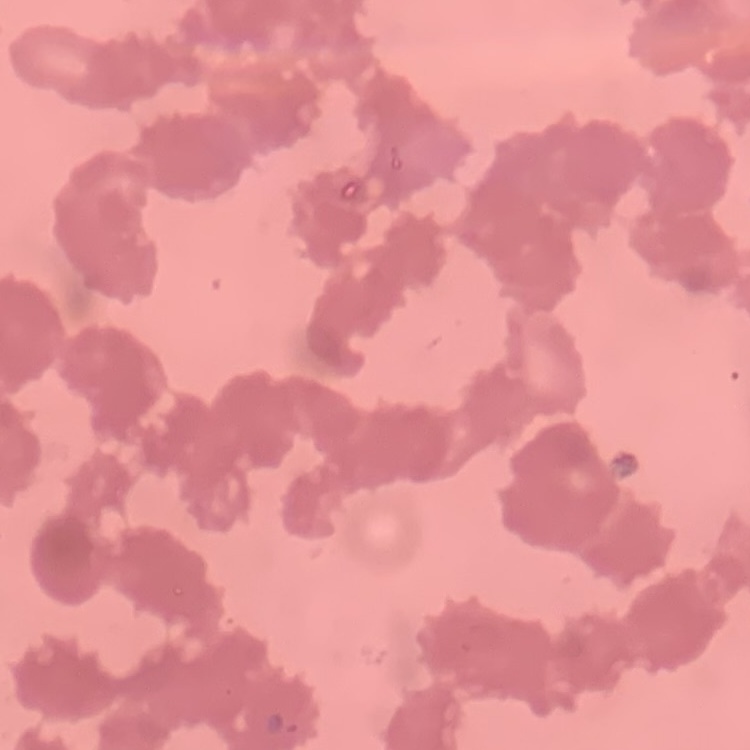

Summary:
  - Red blood cell morphology: rouleaux formation
  - Stain: Field's or Giemsa
  - Preparation: thin blood film
  - Image type: square crop of a larger photomicrograph